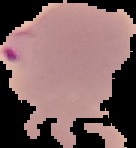

Cell region segmented out of the field of view; the surrounding area is masked to black. Image is 136×148 pixels. From a thin blood film. Malaria status: parasitized.